Identify the preparation type.
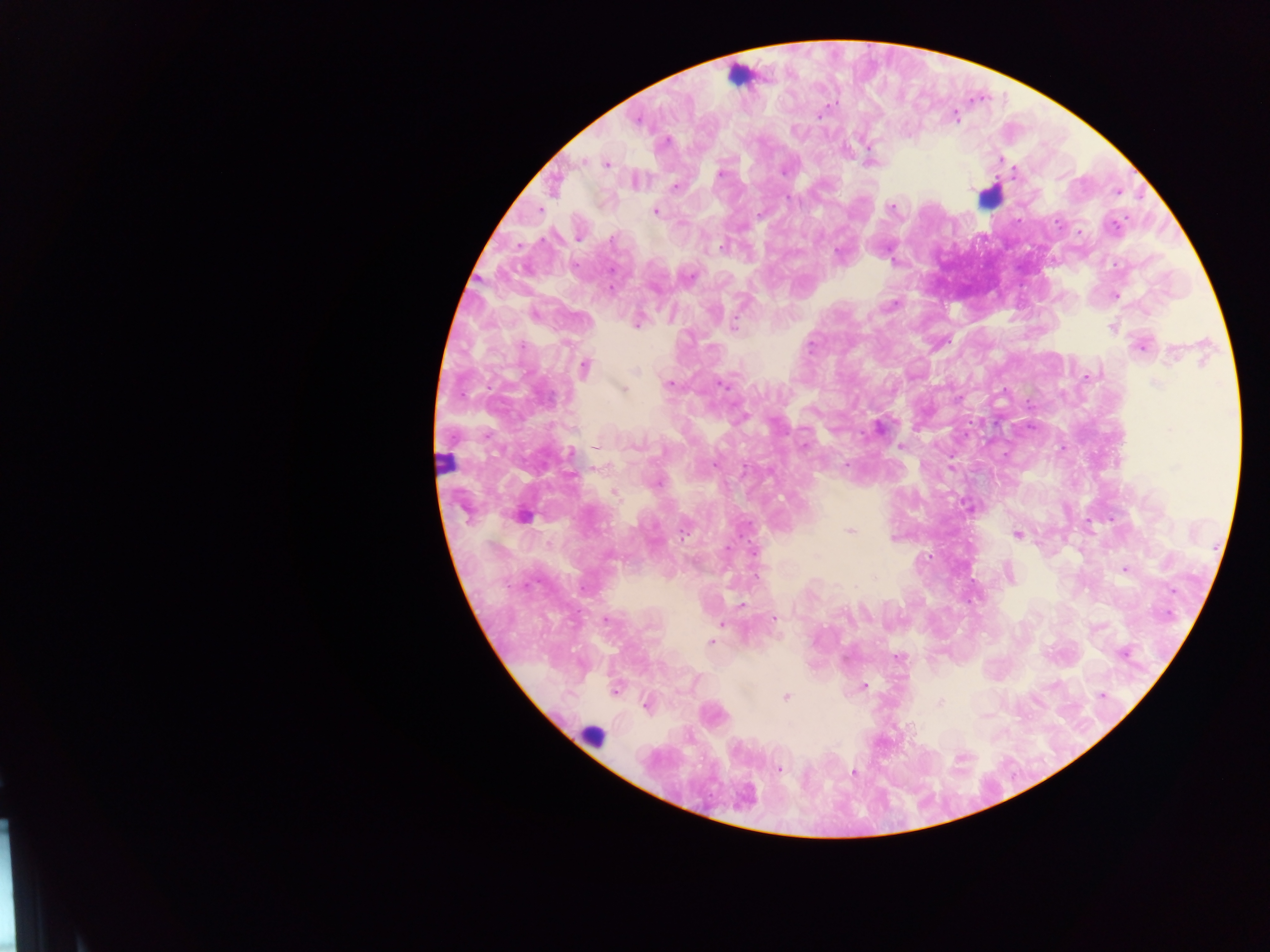
This is a thick smear.

Approximate centers as x y in pixels.
Summary:
  - Plasmodium parasite locations: 821 115; 955 117; 637 120; 666 141; 869 146; 1000 159; 581 162; 606 164; 1014 170; 783 172; 720 174; 675 187; 892 207; 656 211; 759 214; 1057 224; 1116 225; 1079 232; 578 238; 613 238; 722 246; 838 253; 689 277; 611 288; 1115 295; 892 305; 636 324; 734 325; 1112 327; 522 345; 812 345; 1140 347; 1173 355; 585 367; 636 371; 1087 376; 669 384; 720 384; 1156 384; 623 389; 959 398; 742 417; 879 426; 595 445; 634 445; 804 445; 901 446; 571 453; 714 465; 846 465; 656 483; 614 492; 523 516; 850 531; 684 533; 1018 535; 892 539; 728 548; 1125 570; 1010 573; 875 578; 584 588; 1172 591; 742 604; 774 618; 605 620; 721 624; 710 641; 1123 655; 897 657; 864 686; 615 691; 1102 696; 785 697; 941 702; 646 705; 779 770; 853 772
  - Leukocyte locations: 738 75; 988 196; 445 460; 592 736
  - Country: Ghana
  - Capture: mobile-phone photograph through a microscope
  - Image size: 1270×952 pixels
  - Field of view: single